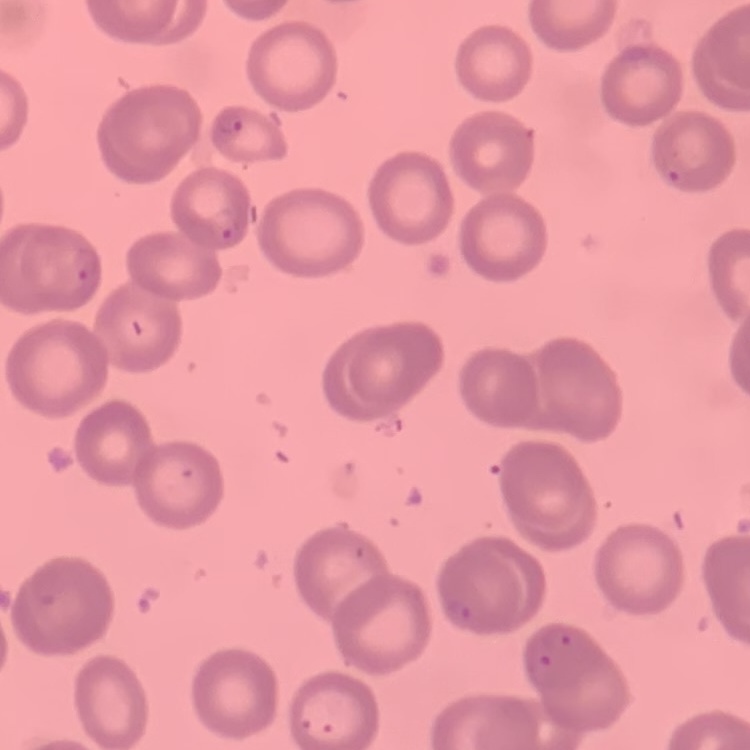 The erythrocytes show no rouleaux formation. Stained with either Field's or Giemsa. Thin peripheral smear. One tile cut from a larger photomicrograph.